Describe the morphology of the red blood cells.
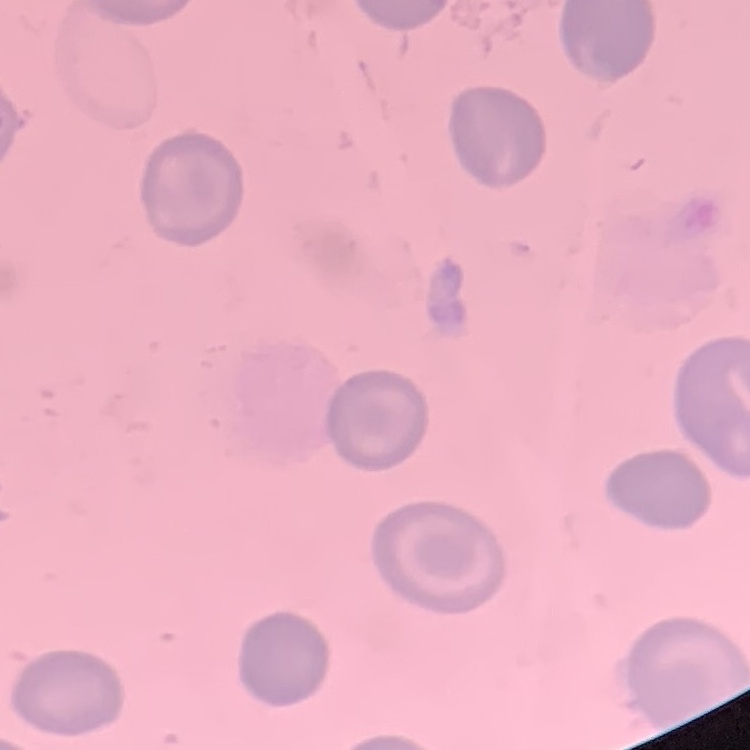
They show no rouleaux formation.

stain = Field's or Giemsa
preparation = thin peripheral smear
image type = one tile cut from a larger photomicrograph